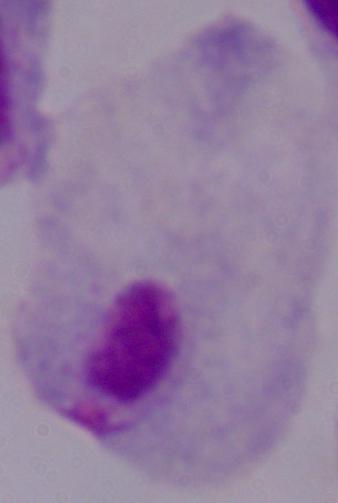
Summary:
  - Magnification: 1000x
  - Modality: photomicrograph
  - Identification: trichomonad